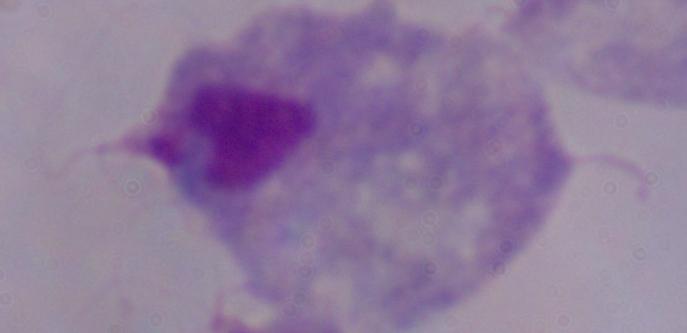
{
  "identification": "trichomonad",
  "magnification": "1000x",
  "modality": "photomicrograph"
}